Classify this cell by malaria status.
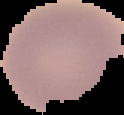
Uninfected.

Summary:
  - Image type: segmented cell region on a black background
  - Preparation: thin blood smear
  - Image size: 124×115 pixels